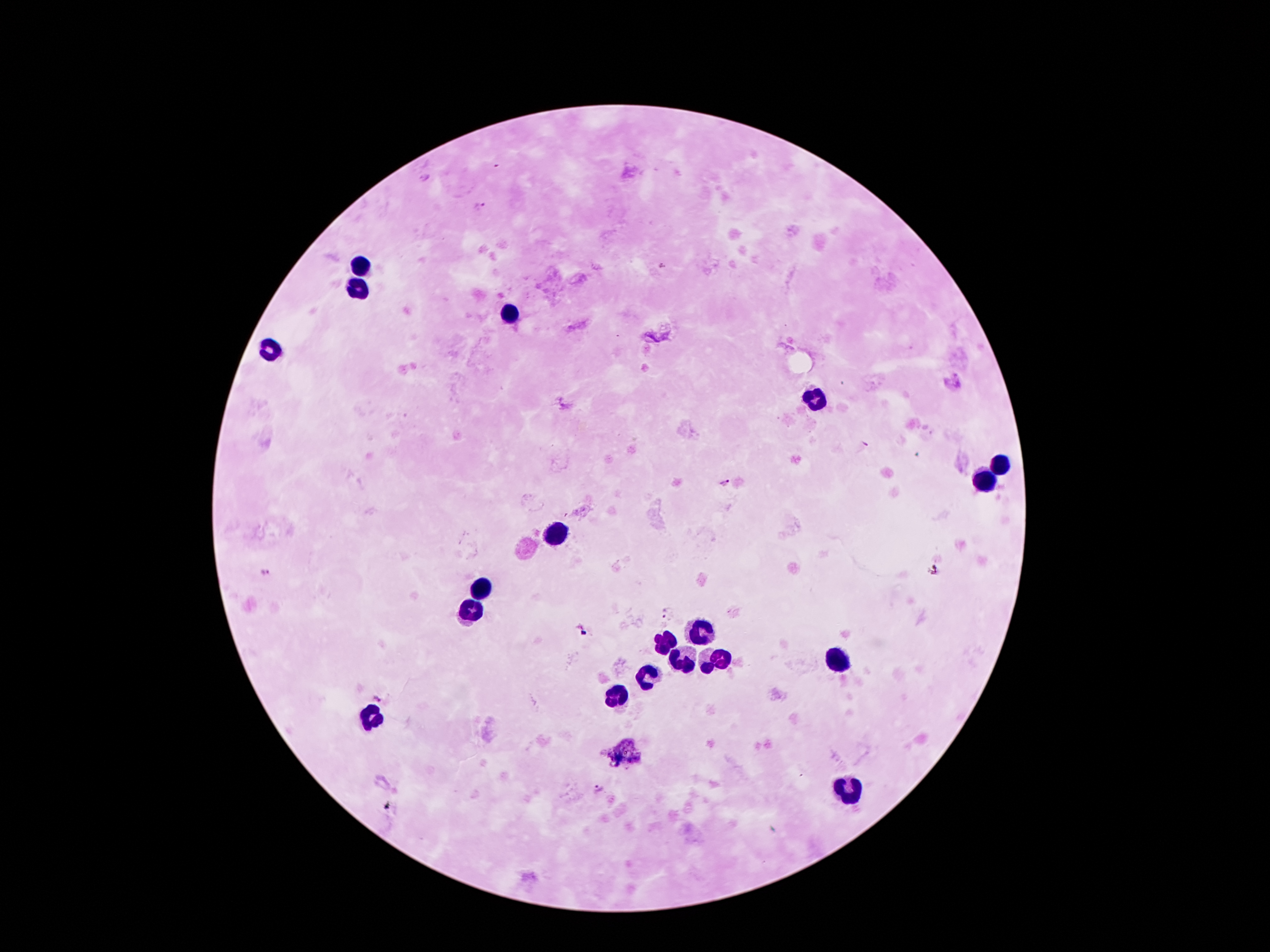

coordinate format = approximate centers as (x, y) in pixels
malaria parasite locations = (479, 209), (725, 483), (934, 568), (266, 572), (667, 612), (380, 696), (600, 790)
leukocyte locations = (363, 264), (358, 291), (506, 311), (271, 350), (819, 396), (1000, 464), (991, 480), (556, 533), (478, 586), (472, 612), (701, 628), (666, 642), (837, 658), (679, 660), (715, 660), (646, 678), (618, 691), (374, 716), (849, 788)
magnification = 100x
image size = 1270×952 pixels
field of view = single
preparation = thick peripheral-blood smear
patient malaria status = infected with Plasmodium falciparum
capture = smartphone through the microscope eyepiece
stain = Giemsa